Mark where platelets are.
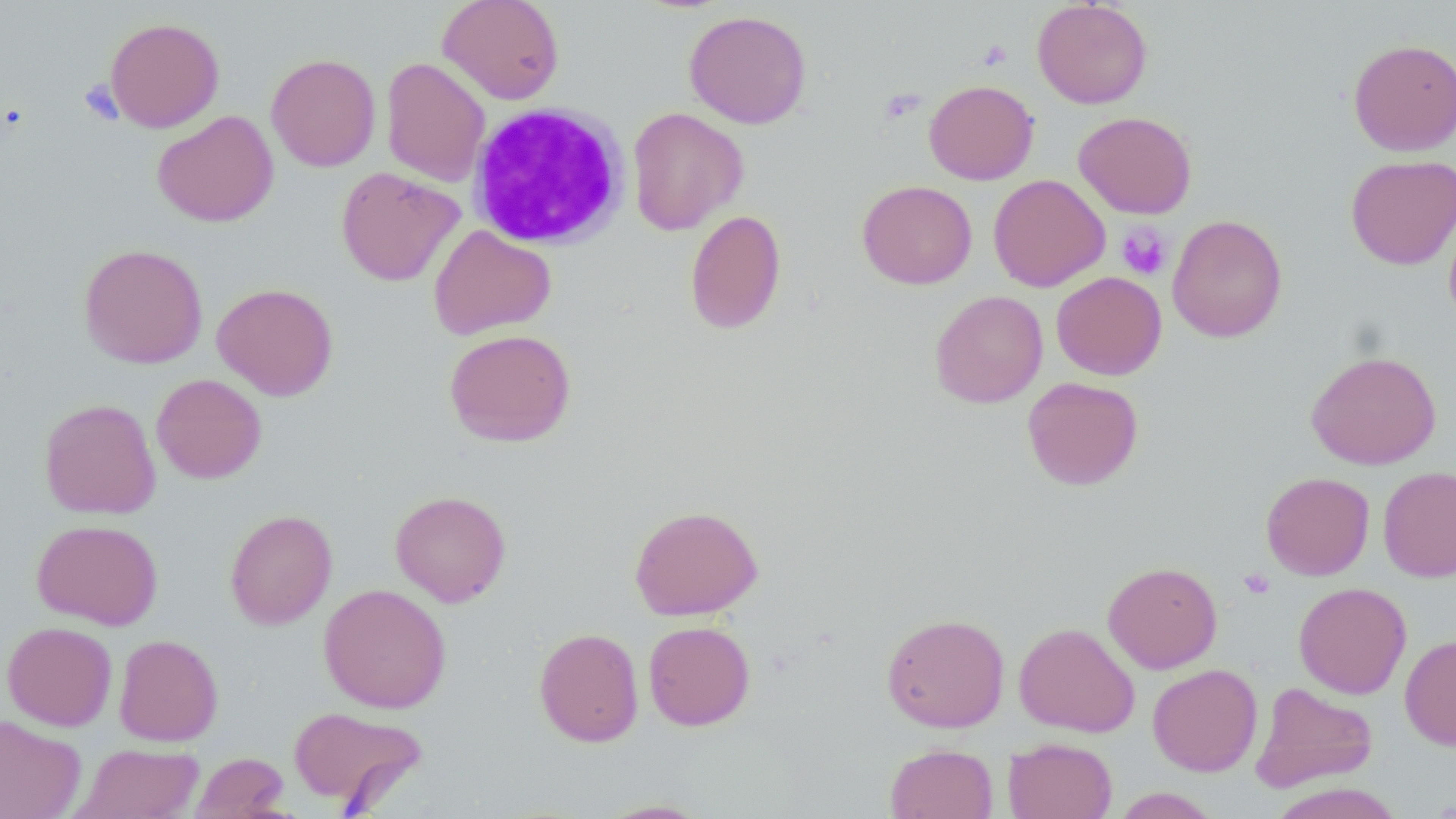
Approximate bounding boxes as (x1, y1, x2, y2) in pixels.
Platelets: (977, 40, 1012, 71), (78, 79, 123, 125), (880, 88, 925, 124), (1116, 222, 1173, 281), (1238, 568, 1275, 599).

slide-level diagnosis = negative for blood parasites
stain = May-Grünwald-Giemsa
modality = optical microscopy
image size = 1456×819 pixels
magnification = 1000x
preparation = thin blood smear
field of view = single
white blood cell locations = approximate bounding boxes as (x1, y1, x2, y2) in pixels: (467, 102, 630, 250)
uninfected red blood cell locations = approximate bounding boxes as (x1, y1, x2, y2) in pixels: (437, 0, 565, 105), (1032, 0, 1152, 109), (684, 10, 812, 129), (104, 17, 225, 132), (1347, 38, 1456, 157), (266, 53, 381, 171), (381, 57, 490, 187), (923, 79, 1038, 185), (626, 107, 748, 235), (152, 110, 279, 227), (1073, 111, 1197, 218), (1345, 155, 1456, 270), (335, 166, 465, 287), (988, 174, 1110, 292), (857, 180, 977, 289), (1443, 209, 1456, 331), (684, 210, 786, 335), (1167, 214, 1288, 343), (428, 224, 557, 340), (79, 243, 208, 368), (1051, 272, 1167, 380), (211, 282, 338, 400), (929, 289, 1048, 407), (443, 328, 576, 447), (1306, 350, 1441, 470), (151, 373, 267, 483), (1022, 377, 1143, 491), (39, 398, 161, 519), (1378, 466, 1456, 581), (1261, 472, 1375, 580), (389, 490, 511, 606), (629, 504, 763, 620), (224, 509, 337, 629), (31, 519, 163, 629), (1103, 561, 1222, 673), (1293, 582, 1412, 698), (318, 583, 452, 713), (880, 612, 1010, 732), (642, 620, 756, 731), (2, 621, 118, 730), (1014, 622, 1140, 737), (533, 627, 644, 747), (114, 633, 223, 746), (1399, 633, 1456, 750), (1147, 663, 1262, 777), (1250, 681, 1378, 793), (288, 706, 429, 811), (0, 714, 86, 819), (1003, 737, 1117, 819), (70, 743, 204, 819), (885, 743, 998, 819), (189, 752, 291, 818), (1268, 782, 1407, 819), (1111, 788, 1222, 818), (593, 798, 715, 818)